Name the cell type shown.
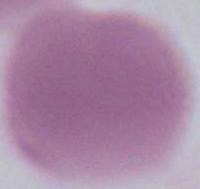
This is an erythrocyte.

magnification = 1000x
modality = photomicrograph